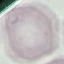

Summary:
  - Malaria status: uninfected
  - Capture: smartphone camera at the microscope eyepiece
  - Preparation: thin blood smear
  - Image type: automatically extracted cell patch, resized to 64 × 64 pixels
  - Stain: Giemsa